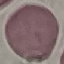 Result: no malaria parasites seen. Thin smear of blood. Automatically extracted cell patch, resized to 64 × 64 pixels. Photographed with a smartphone camera at the microscope eyepiece. Giemsa-stained preparation.